State the blood parasite species.
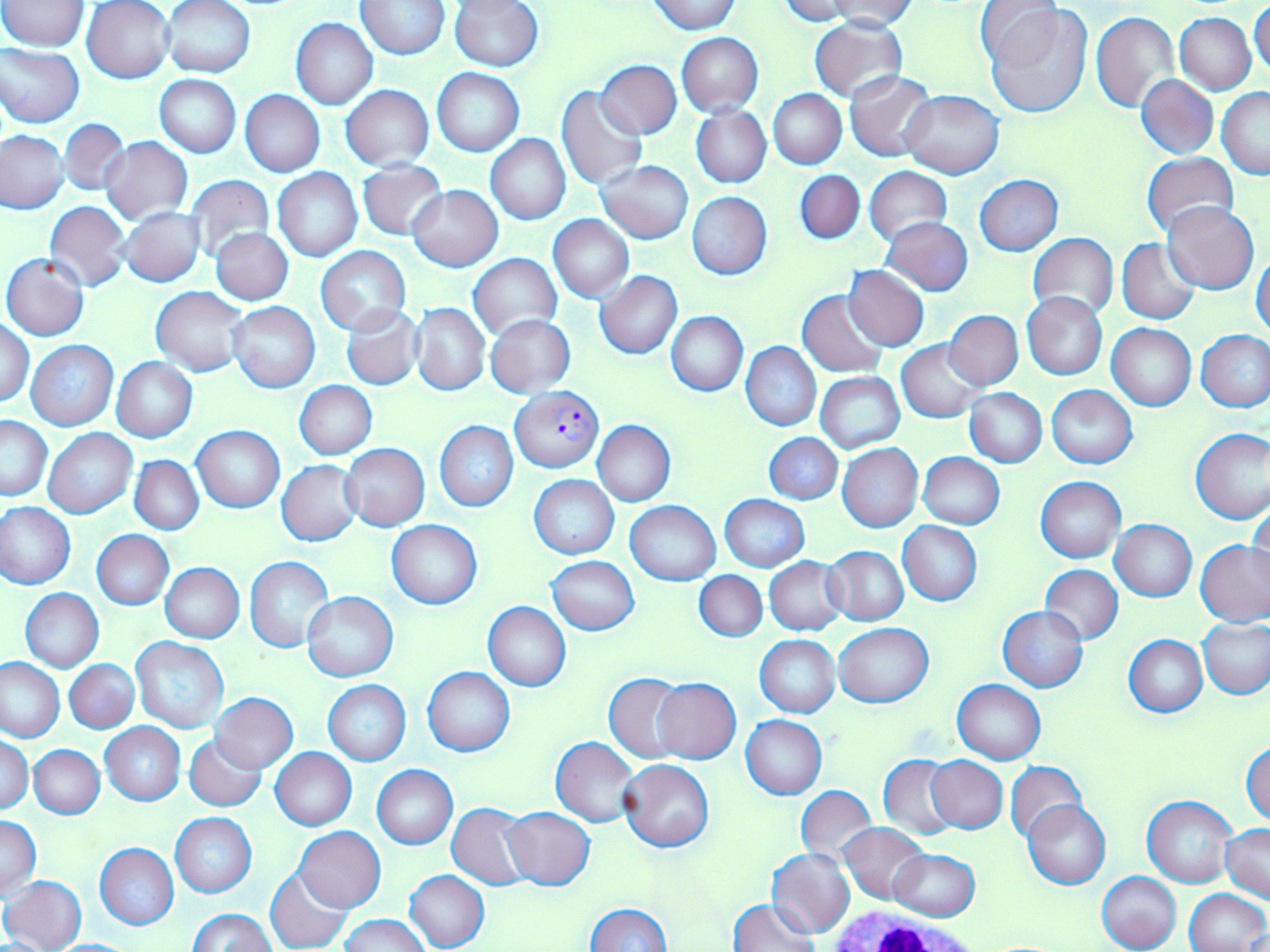

Plasmodium falciparum.

magnification: 1000x
stain: May-Grünwald-Giemsa
image_size: 1270×952 pixels
plasmodium_falciparum_infected_red_blood_cell_locations: 'approximate bounding boxes as (x1, y1, x2, y2) in pixels: (512, 385, 604, 472)'
modality: optical microscopy
field_of_view: single
white_blood_cell_locations: 'approximate bounding boxes as (x1, y1, x2, y2) in pixels: (830, 904, 983, 952)'
preparation: thin blood film
uninfected_red_blood_cell_locations: 'approximate bounding boxes as (x1, y1, x2, y2) in pixels: (162, 0, 256, 78), (648, 0, 741, 34), (776, 0, 859, 24), (1, 1, 89, 51), (83, 1, 175, 83), (355, 1, 449, 59), (449, 1, 544, 71), (823, 1, 917, 31), (982, 3, 1092, 118), (1250, 3, 1270, 81), (977, 4, 1062, 71), (1090, 12, 1180, 114), (1175, 13, 1256, 95), (810, 16, 907, 103), (290, 18, 378, 109), (676, 33, 763, 117), (0, 45, 84, 127), (598, 60, 682, 138), (432, 68, 524, 156), (846, 70, 936, 161), (1136, 73, 1217, 159), (156, 75, 241, 157), (340, 85, 433, 171), (555, 86, 648, 191), (1217, 87, 1270, 178), (768, 89, 845, 170), (240, 90, 324, 177), (901, 90, 1004, 179), (691, 108, 772, 187), (58, 119, 130, 196), (0, 129, 69, 213), (485, 134, 571, 225), (101, 135, 192, 225), (1142, 152, 1238, 238), (597, 159, 693, 244), (356, 161, 447, 240), (864, 167, 952, 244), (273, 169, 363, 262), (794, 170, 865, 245), (184, 174, 275, 262), (975, 175, 1064, 256), (408, 185, 502, 271), (687, 192, 772, 279), (43, 201, 132, 291), (1164, 202, 1259, 293), (119, 208, 205, 286), (549, 215, 634, 303), (881, 217, 972, 296), (211, 229, 293, 305), (1028, 233, 1118, 321), (1118, 239, 1201, 325), (315, 246, 410, 335), (1252, 250, 1270, 339), (468, 253, 561, 338), (2, 254, 89, 342), (844, 265, 929, 351), (596, 271, 682, 359), (150, 286, 249, 375), (797, 289, 889, 378), (1022, 292, 1108, 380), (228, 302, 320, 393), (412, 303, 490, 395), (342, 305, 423, 389), (944, 310, 1023, 390), (665, 311, 749, 396), (485, 314, 576, 396), (1, 318, 34, 408), (1107, 324, 1195, 410), (1196, 330, 1270, 414), (897, 339, 986, 422), (25, 340, 118, 431), (742, 341, 821, 431), (111, 358, 198, 443), (816, 372, 905, 453), (295, 381, 376, 459), (1047, 385, 1137, 469), (963, 387, 1047, 467), (1, 415, 52, 500), (434, 421, 518, 511), (592, 421, 675, 507), (193, 426, 285, 513), (43, 428, 137, 518), (1191, 428, 1270, 524), (764, 434, 842, 504), (837, 443, 924, 532), (342, 444, 430, 531), (917, 453, 1003, 529), (130, 456, 204, 535), (278, 460, 363, 547), (530, 475, 618, 560), (1036, 476, 1126, 563), (720, 494, 809, 572), (1249, 500, 1269, 585), (625, 501, 720, 585), (1, 502, 76, 589), (1110, 519, 1197, 601), (386, 520, 481, 608), (898, 521, 982, 606), (92, 530, 173, 609), (1196, 540, 1270, 626), (825, 545, 909, 625), (244, 556, 332, 651), (547, 556, 640, 635), (764, 557, 847, 636), (159, 562, 245, 642), (1041, 565, 1123, 644), (695, 572, 767, 642), (20, 588, 103, 672), (303, 591, 397, 682), (483, 602, 571, 691), (998, 607, 1088, 692), (1198, 618, 1270, 699), (835, 622, 933, 706), (1123, 634, 1207, 718), (756, 636, 840, 717), (131, 638, 230, 734), (0, 657, 64, 742), (66, 659, 138, 732), (422, 666, 516, 756), (605, 673, 693, 763), (653, 679, 741, 764), (324, 680, 411, 766), (952, 680, 1046, 764), (211, 693, 297, 771), (740, 715, 827, 799), (100, 722, 185, 804), (184, 733, 264, 812), (0, 735, 33, 813), (550, 737, 639, 827), (1243, 741, 1270, 826), (31, 745, 105, 818), (270, 748, 356, 830), (879, 755, 960, 839), (926, 755, 1008, 832), (618, 758, 714, 852), (1005, 761, 1087, 845), (372, 765, 458, 849), (796, 784, 877, 867), (1143, 796, 1237, 888), (1024, 801, 1109, 889), (447, 803, 534, 889), (501, 807, 594, 890), (169, 812, 256, 897), (1, 816, 41, 899), (838, 822, 929, 904), (1221, 823, 1269, 901), (295, 827, 384, 912), (95, 843, 178, 929), (768, 847, 855, 937), (890, 850, 980, 921), (265, 866, 353, 952), (404, 870, 490, 951), (1096, 871, 1181, 952), (1, 875, 86, 952), (1185, 888, 1269, 952), (728, 897, 820, 952), (583, 903, 672, 952), (189, 909, 274, 952), (341, 914, 429, 952), (49, 939, 140, 951)'